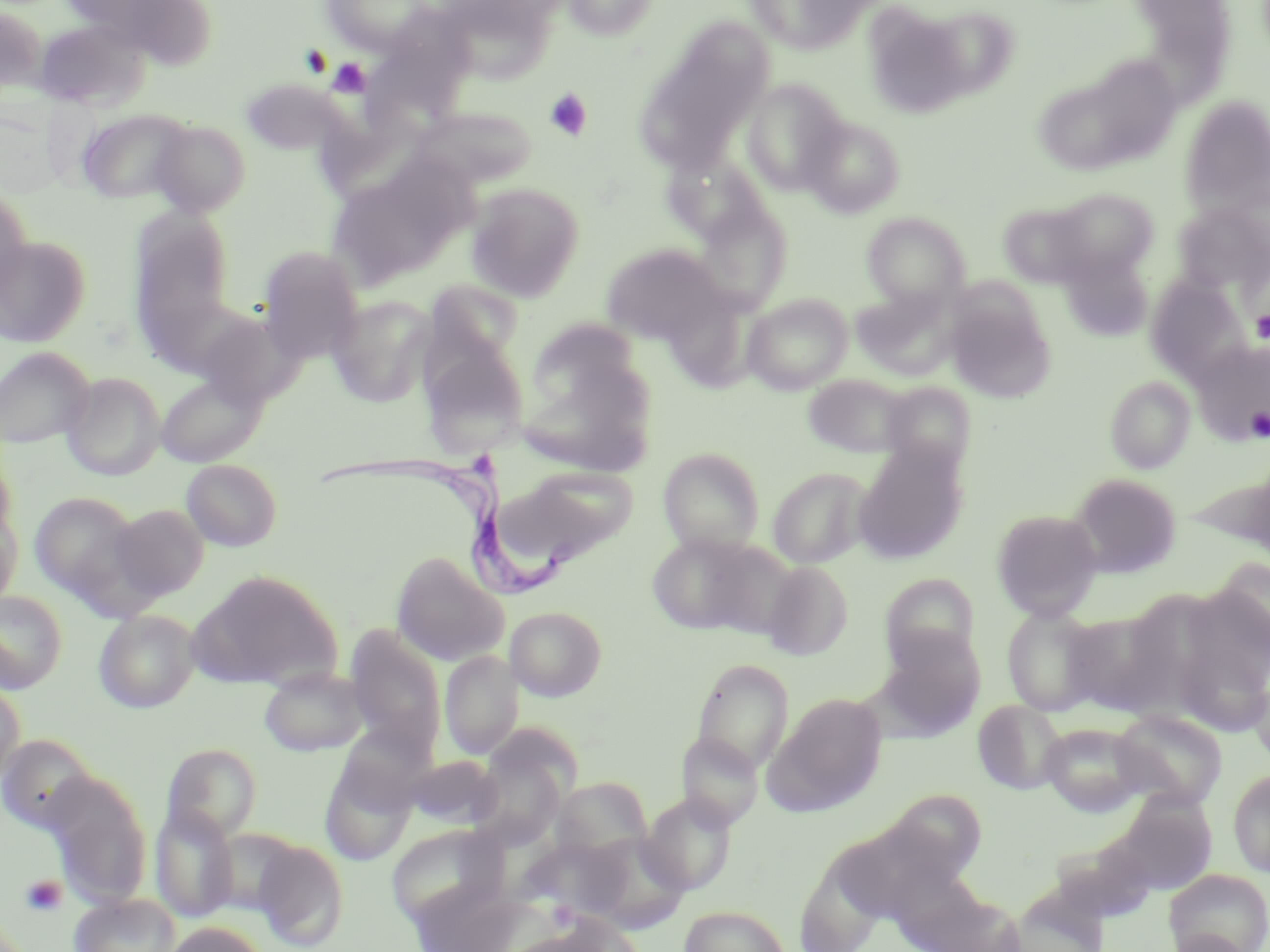

Summary:
  - Coordinate format: approximate bounding boxes as [x1, y1, x2, y2] in pixels
  - Uninfected red blood cell locations: [61, 0, 217, 67], [319, 0, 437, 55], [437, 0, 559, 80], [560, 0, 661, 41], [744, 0, 875, 54], [921, 4, 1021, 99], [0, 5, 46, 96], [863, 5, 977, 120], [34, 18, 152, 110], [634, 23, 773, 172], [1053, 58, 1184, 171], [239, 77, 347, 156], [741, 79, 849, 194], [1180, 96, 1270, 216], [411, 106, 537, 191], [0, 108, 62, 198], [77, 108, 195, 203], [801, 115, 904, 218], [150, 119, 251, 217], [325, 161, 471, 290], [466, 183, 585, 301], [0, 185, 32, 306], [1050, 187, 1159, 281], [691, 195, 792, 315], [998, 200, 1095, 288], [1172, 204, 1269, 297], [126, 210, 238, 356], [862, 212, 971, 311], [0, 236, 91, 347], [600, 243, 729, 345], [257, 247, 365, 363], [1060, 250, 1153, 342], [1145, 276, 1251, 384], [421, 279, 524, 382], [851, 287, 960, 381], [663, 289, 759, 394], [742, 293, 853, 395], [326, 295, 436, 405], [945, 297, 1055, 403], [192, 311, 304, 410], [527, 315, 649, 406], [419, 337, 530, 459], [1191, 339, 1270, 446], [0, 346, 95, 449], [61, 371, 166, 481], [155, 372, 267, 468], [803, 374, 915, 458], [1105, 375, 1195, 473], [880, 381, 977, 474], [520, 394, 653, 474], [853, 443, 968, 564], [658, 447, 765, 555], [0, 450, 17, 549], [181, 458, 283, 551], [1183, 464, 1270, 548], [768, 466, 873, 568], [493, 467, 634, 573], [1069, 472, 1182, 578], [29, 490, 147, 606], [110, 503, 209, 602], [0, 506, 22, 610], [991, 508, 1103, 620], [646, 532, 775, 637], [391, 551, 509, 666], [1205, 558, 1269, 669], [762, 560, 854, 660], [188, 569, 344, 691], [880, 573, 982, 670], [0, 589, 68, 694], [1002, 605, 1107, 716], [505, 606, 607, 701], [1060, 608, 1177, 718], [93, 609, 200, 713], [345, 627, 446, 756], [874, 630, 986, 735], [1171, 635, 1270, 738], [440, 650, 524, 760], [691, 658, 795, 774], [259, 668, 369, 757], [1249, 674, 1270, 766], [0, 681, 26, 789], [769, 693, 887, 812], [972, 699, 1069, 796], [1110, 709, 1228, 808], [333, 722, 435, 817], [1040, 722, 1152, 815], [676, 731, 765, 829], [0, 736, 95, 833], [161, 743, 262, 844], [404, 755, 502, 829], [320, 757, 416, 866], [477, 766, 564, 855], [1228, 767, 1270, 878], [42, 771, 152, 909], [552, 776, 653, 861], [871, 790, 989, 887], [1110, 790, 1220, 897], [640, 793, 738, 895], [151, 805, 238, 923], [386, 823, 507, 926], [580, 832, 690, 933], [523, 835, 636, 917], [835, 835, 941, 923], [253, 840, 349, 951], [1054, 845, 1154, 923], [1164, 869, 1270, 952], [923, 888, 1027, 952], [69, 893, 181, 952], [679, 904, 791, 952], [163, 921, 269, 952], [1162, 930, 1253, 952]
  - Platelet locations: [327, 57, 373, 97], [545, 88, 593, 141], [1249, 310, 1270, 343], [1246, 407, 1270, 441], [21, 875, 67, 916], [547, 901, 580, 928]
  - Trypanosoma brucei locations: [320, 453, 575, 600]
  - Slide-level diagnosis: Trypanosoma brucei
  - Magnification: 1000x
  - Field of view: single
  - Modality: optical microscopy
  - Stain: May-Grünwald-Giemsa
  - Preparation: thin blood film
  - Image size: 1270×952 pixels